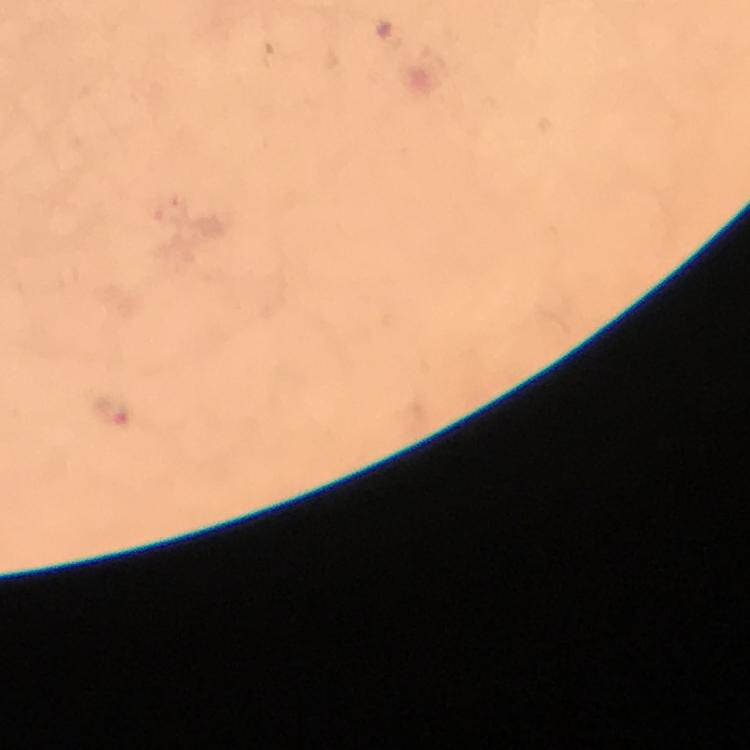
Approximate object centers, in pixels from the top-left corner. Malaria parasite locations: (x=111, y=413). Image is 750×750 pixels. Immersion oil was used. Thick blood smear. Giemsa-stained preparation. Photographed with a smartphone mounted on the microscope. 100x magnification. Cropped region of a single field of view. From a malaria diagnostic workup.